Point out each Plasmodium parasite.
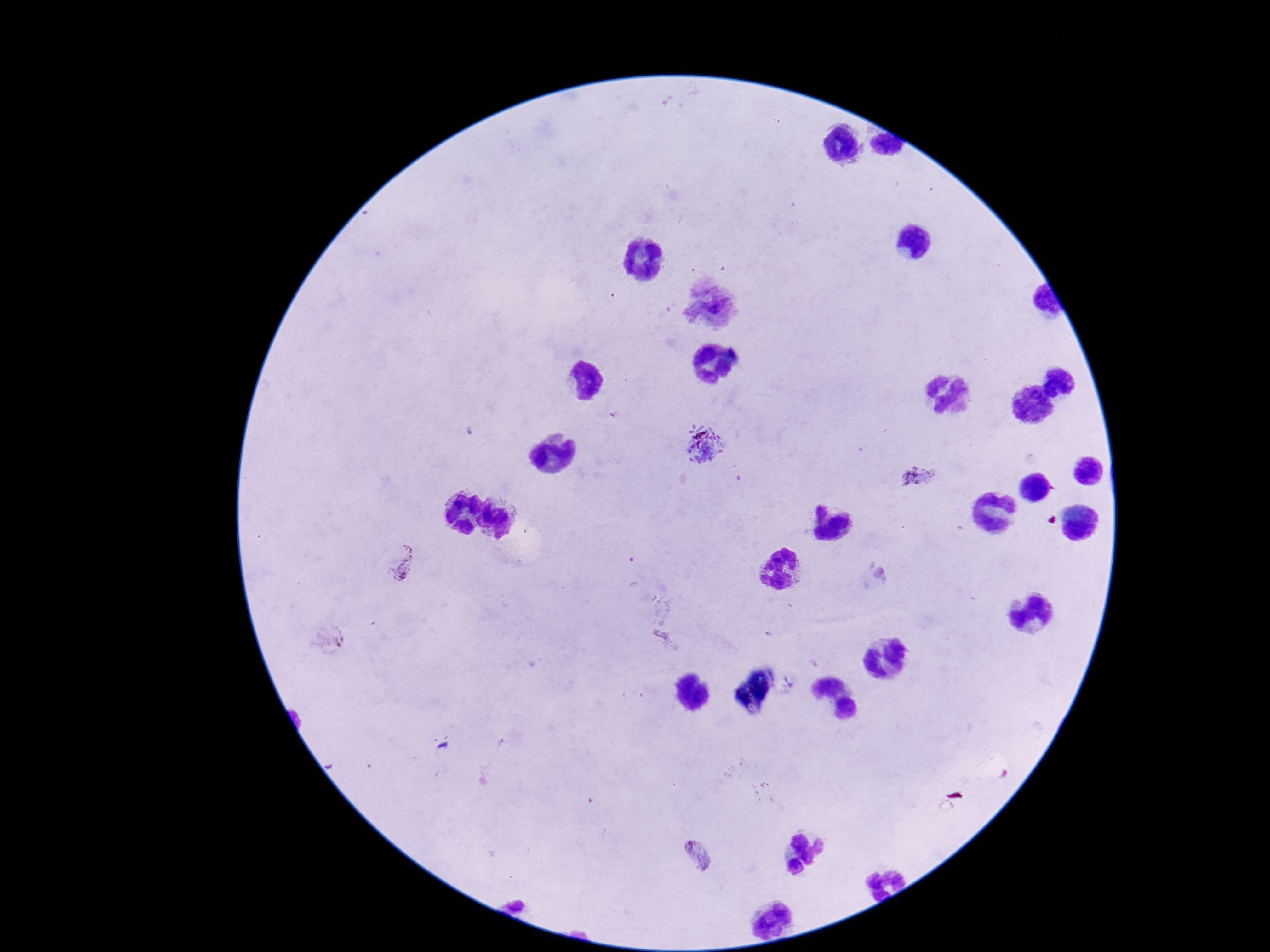
Approximate centers as {x, y} in pixels.
Plasmodium parasites: {705, 445}, {920, 476}, {400, 561}, {877, 575}, {698, 853}.

Patient malaria status: positive. Single field of view. 100x magnification. Photographed through the microscope eyepiece with a smartphone camera. Thick peripheral-blood smear. Image is 1270×952 pixels. Giemsa-stained preparation.